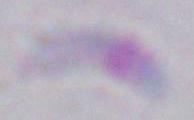 Photomicrograph. Captured at 1000x magnification. Toxoplasma gondii is seen.